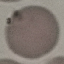
Summary:
  - Result: no malaria parasites seen
  - Stain: Giemsa
  - Image type: automatically extracted cell patch, resized to 64 × 64 pixels
  - Preparation: thin smear
  - Capture: smartphone through the microscope eyepiece